Assess the morphology of the red blood cells.
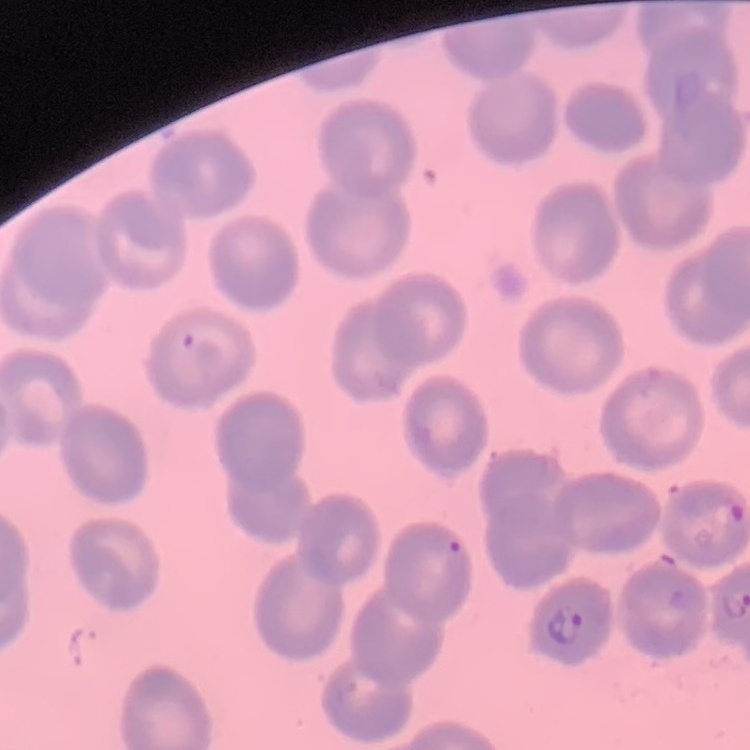
No rouleaux formation.

Summary:
  - Image type: square crop of a larger photomicrograph
  - Stain: Field's or Giemsa
  - Preparation: thin blood film